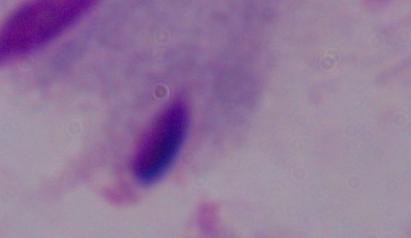
Captured at 1000x magnification. Photomicrograph. A trichomonad is shown.